Locate every malaria parasite.
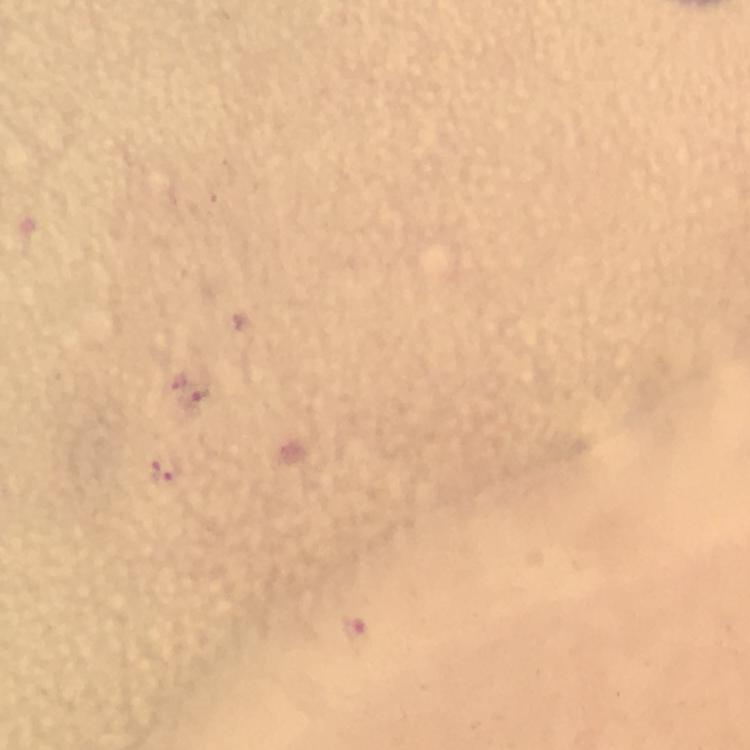

Approximate object centers, in pixels from the top-left corner.
Malaria parasites: (x=194, y=397), (x=160, y=474), (x=353, y=631).

Summary:
  - Context: from a diagnostic examination for malaria
  - Image size: 750×750 pixels
  - Stain: Giemsa
  - Preparation: thick smear
  - Magnification: 100x
  - Cropped from: one field of view
  - Immersion oil: applied
  - Capture: smartphone mounted on the microscope